Locate every Trypanosoma brucei.
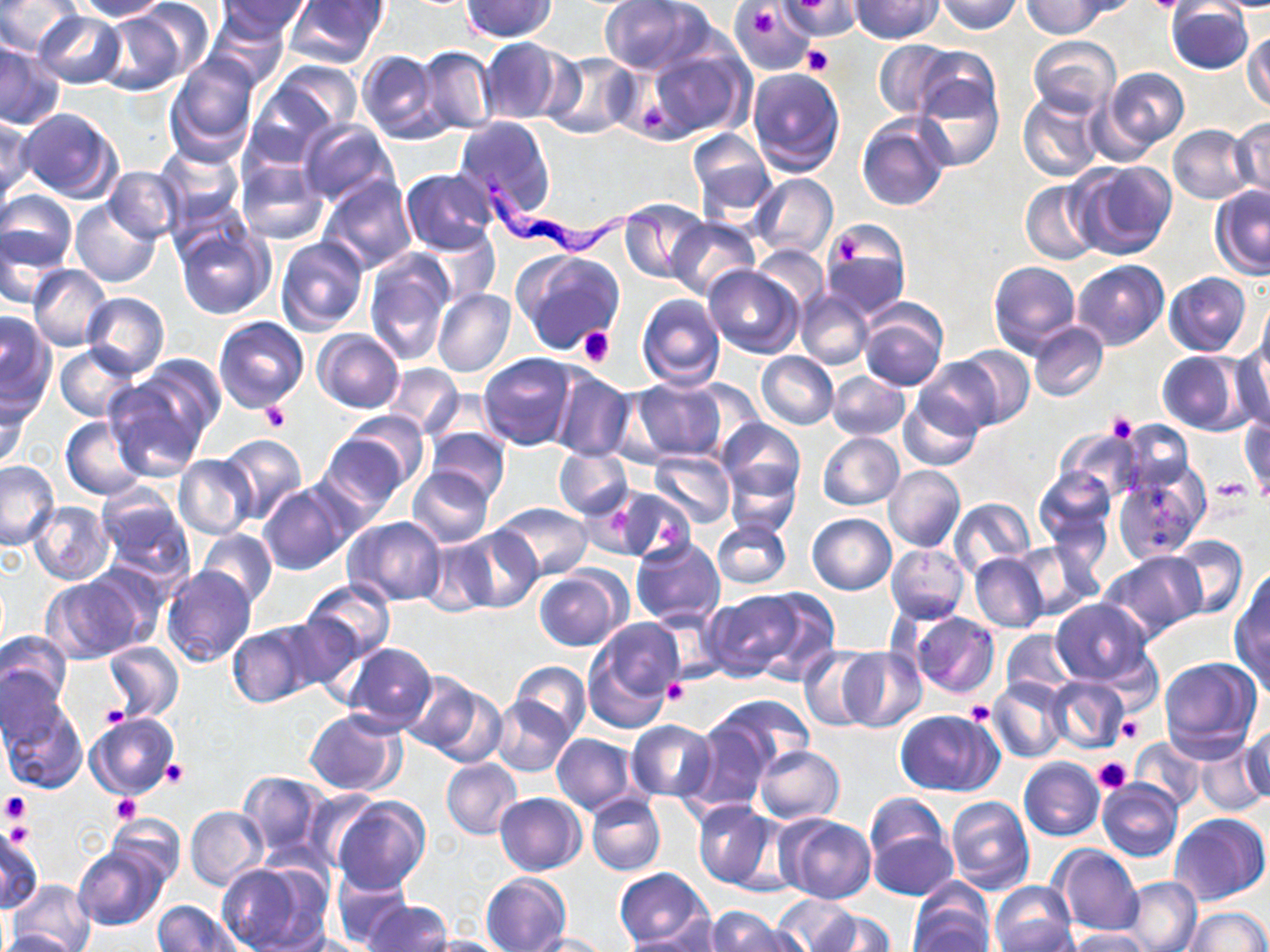
Approximate bounding boxes as (x1,y1)-(x2,y2) corner pairs in pixels.
Trypanosoma brucei: (479,173)-(684,277).

slide-level diagnosis = Trypanosoma brucei
image size = 1270×952 pixels
stain = May-Grünwald-Giemsa
preparation = thin blood smear
uninfected red blood cell locations = approximate bounding boxes as (x1,y1)-(x2,y2) corner pairs in pixels: (0,0)-(79,55), (71,0)-(170,21), (218,0)-(312,40), (284,0)-(389,69), (851,0)-(942,43), (938,0)-(1021,34), (1062,0)-(1144,20), (462,1)-(557,41), (600,1)-(700,74), (783,1)-(861,41), (1022,1)-(1107,38), (134,2)-(215,83), (731,2)-(815,73), (1167,3)-(1253,74), (96,9)-(188,96), (203,9)-(290,91), (34,11)-(126,88), (1244,27)-(1270,113), (1028,36)-(1121,116), (477,37)-(572,125), (874,40)-(956,117), (0,44)-(66,129), (648,46)-(752,139), (909,46)-(1000,126), (416,47)-(495,134), (357,49)-(445,142), (542,51)-(640,137), (166,55)-(260,160), (272,60)-(361,133), (747,65)-(845,176), (1100,67)-(1189,156), (913,78)-(1003,172), (242,81)-(337,169), (1017,91)-(1104,183), (17,107)-(122,203), (856,115)-(949,211), (1,116)-(34,204), (453,116)-(556,221), (296,118)-(397,208), (1230,118)-(1270,200), (1168,124)-(1253,203), (688,129)-(775,217), (155,145)-(244,228), (236,159)-(329,247), (1072,160)-(1176,259), (104,166)-(181,243), (401,168)-(498,254), (751,173)-(838,259), (320,175)-(417,273), (1020,180)-(1102,264), (1209,184)-(1269,277), (0,190)-(77,273), (70,200)-(161,287), (621,202)-(707,284), (666,217)-(760,301), (175,226)-(275,319), (0,227)-(66,311), (419,227)-(498,308), (821,227)-(908,317), (275,237)-(369,337), (752,245)-(827,312), (364,250)-(454,363), (513,250)-(624,356), (989,260)-(1082,357), (1072,260)-(1169,350), (27,266)-(112,349), (703,266)-(803,359), (1164,272)-(1252,356), (433,287)-(515,377), (795,289)-(874,371), (81,292)-(169,376), (637,293)-(725,389), (1258,295)-(1270,375), (858,303)-(949,391), (0,311)-(57,415), (213,315)-(309,411), (1028,321)-(1107,401), (312,328)-(404,413), (1230,341)-(1270,435), (55,344)-(141,422), (954,346)-(1036,428), (757,351)-(839,429), (1155,351)-(1245,434), (479,353)-(577,450), (127,354)-(226,454), (915,357)-(1004,437), (383,360)-(465,438), (548,369)-(634,462), (828,370)-(909,441), (104,376)-(211,481), (677,377)-(768,458), (630,378)-(727,461), (427,388)-(500,453), (0,390)-(33,473), (899,390)-(983,470), (333,411)-(429,495), (1240,414)-(1269,498), (61,416)-(148,500), (718,419)-(805,499), (1118,420)-(1195,497), (425,427)-(510,503), (1058,427)-(1143,499), (818,431)-(904,511), (217,434)-(308,524), (318,434)-(410,516), (554,447)-(633,518), (650,450)-(736,528), (175,455)-(256,540), (725,459)-(802,539), (0,460)-(59,550), (884,464)-(966,553), (1113,464)-(1208,562), (406,466)-(494,548), (1033,467)-(1115,554), (259,483)-(351,575), (94,484)-(192,582), (609,485)-(694,564), (948,498)-(1034,577), (26,501)-(115,585), (495,501)-(594,579), (807,513)-(896,594), (343,515)-(444,606), (711,519)-(791,589), (452,525)-(543,614), (198,529)-(278,607), (1166,535)-(1248,620), (630,537)-(724,626), (418,538)-(501,616), (1013,541)-(1101,620), (887,544)-(970,623), (1099,551)-(1205,641), (970,552)-(1050,632), (162,566)-(256,669), (535,569)-(627,651), (1230,575)-(1270,687), (41,576)-(141,663), (302,578)-(395,664), (700,590)-(801,681), (749,590)-(841,684), (1051,599)-(1154,686), (909,611)-(999,698), (227,622)-(320,707), (582,625)-(683,734), (1000,629)-(1077,700), (1,630)-(72,716), (103,642)-(183,723), (343,642)-(436,731), (800,646)-(881,731), (839,647)-(926,731), (1159,656)-(1262,761), (510,662)-(590,739), (0,663)-(66,749), (1045,675)-(1129,756), (416,676)-(507,767), (988,678)-(1070,763), (712,693)-(815,775), (490,695)-(577,776), (2,704)-(88,795), (893,709)-(1002,796), (304,710)-(406,796), (85,712)-(180,801), (627,719)-(717,802), (681,719)-(777,813), (1242,724)-(1270,806), (551,734)-(637,813), (1129,736)-(1207,813), (1194,740)-(1268,815), (753,745)-(845,825), (1017,757)-(1104,841), (441,758)-(523,840), (238,771)-(327,857), (1096,778)-(1183,863), (303,789)-(383,871), (495,792)-(587,875), (587,792)-(666,875), (333,797)-(429,894), (945,797)-(1034,894), (692,799)-(785,892), (866,801)-(956,899), (186,805)-(268,890), (108,812)-(184,887), (1171,813)-(1268,906), (777,814)-(877,905), (0,828)-(44,912), (1050,843)-(1142,935), (73,845)-(167,930), (215,862)-(323,951), (614,868)-(711,948), (329,869)-(413,946), (481,873)-(571,952), (1123,876)-(1202,952), (8,880)-(95,952), (991,883)-(1076,950), (909,884)-(994,952), (770,895)-(862,951), (153,900)-(240,951), (363,901)-(452,952), (1182,906)-(1269,951), (706,907)-(804,952), (805,909)-(895,952), (1066,928)-(1153,951), (617,929)-(722,952), (0,930)-(77,952), (278,933)-(367,951), (519,933)-(613,952), (418,936)-(513,952)
modality = light microscopy
magnification = 1000x
platelet locations = approximate bounding boxes as (x1,y1)-(x2,y2) corner pairs in pixels: (785,0)-(852,46), (1142,0)-(1186,13), (750,7)-(779,38), (804,44)-(834,75), (579,326)-(615,365), (259,403)-(292,432), (1107,411)-(1138,442), (1209,479)-(1253,504), (665,680)-(690,706), (965,702)-(995,725), (99,705)-(127,731), (1115,713)-(1145,744), (1093,756)-(1133,794), (160,759)-(186,788), (0,790)-(31,822), (111,792)-(139,822), (4,820)-(34,847)
field of view = one of a larger specimen